Assess the morphology of the erythrocytes.
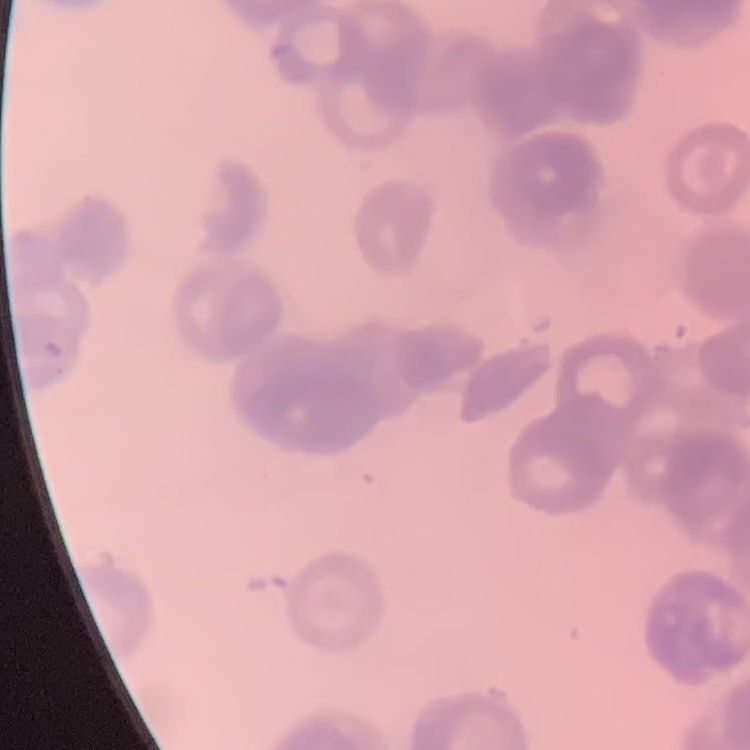
They show rouleaux formation.

Summary:
  - Image type: square crop of a larger photomicrograph
  - Preparation: thin blood film
  - Stain: Field's or Giemsa